Identify the blood parasite species.
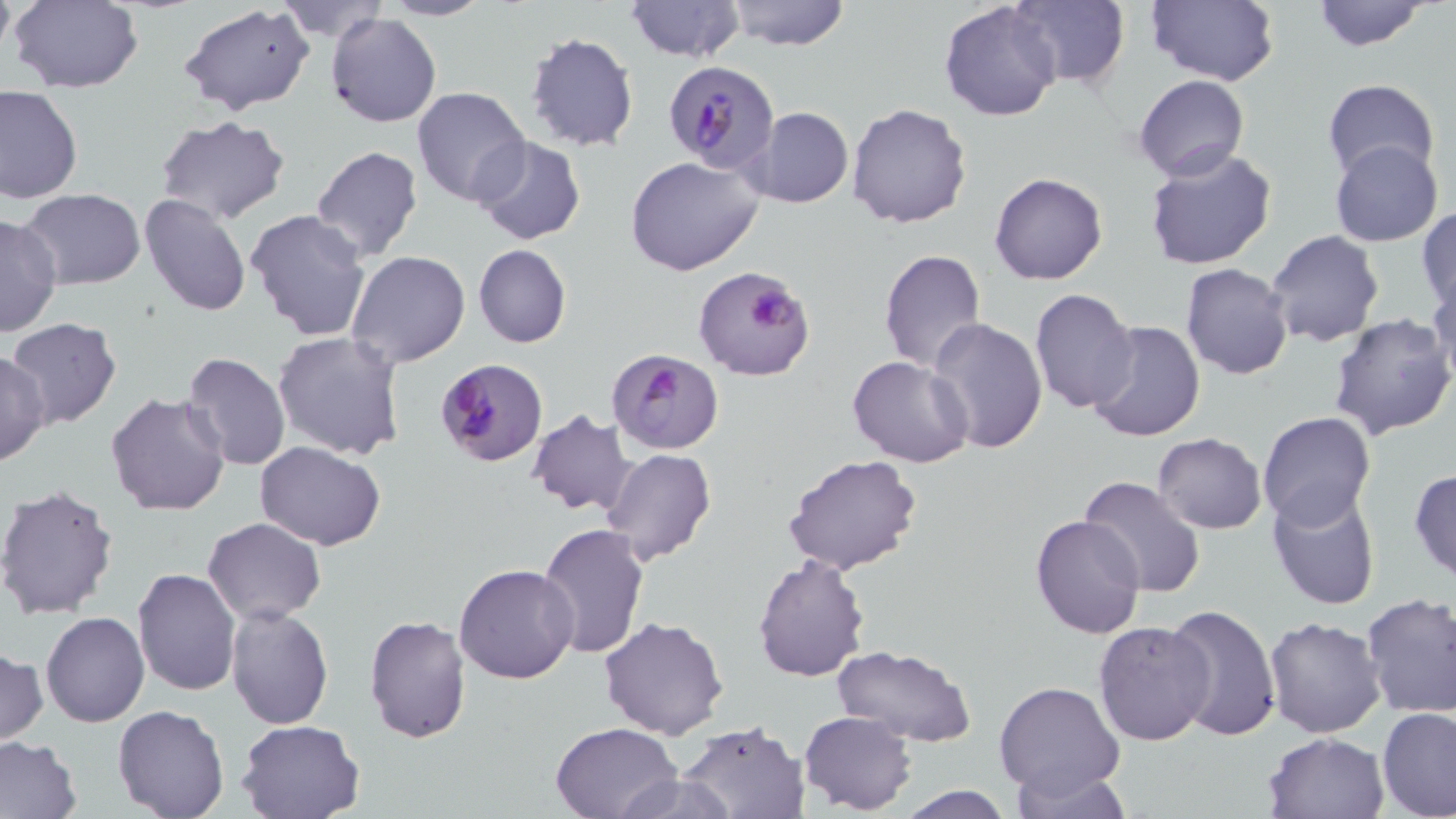

Plasmodium falciparum.

Summary:
  - Coordinate format: approximate bounding boxes as named x1/y1/x2/y2 corners in pixels
  - Uninfected red blood cell locations: (x1=8, y1=0, x2=144, y2=93), (x1=274, y1=0, x2=389, y2=42), (x1=381, y1=0, x2=492, y2=21), (x1=624, y1=0, x2=745, y2=63), (x1=724, y1=0, x2=851, y2=50), (x1=1009, y1=0, x2=1130, y2=88), (x1=1147, y1=0, x2=1279, y2=86), (x1=1310, y1=0, x2=1433, y2=51), (x1=940, y1=1, x2=1063, y2=122), (x1=180, y1=3, x2=316, y2=114), (x1=326, y1=11, x2=442, y2=128), (x1=524, y1=32, x2=638, y2=153), (x1=1135, y1=74, x2=1249, y2=183), (x1=1320, y1=78, x2=1440, y2=183), (x1=0, y1=85, x2=83, y2=204), (x1=412, y1=86, x2=530, y2=208), (x1=846, y1=103, x2=972, y2=229), (x1=741, y1=107, x2=855, y2=208), (x1=155, y1=116, x2=293, y2=224), (x1=470, y1=136, x2=586, y2=245), (x1=1330, y1=139, x2=1443, y2=247), (x1=310, y1=146, x2=424, y2=263), (x1=1144, y1=146, x2=1278, y2=270), (x1=627, y1=157, x2=766, y2=277), (x1=990, y1=172, x2=1108, y2=286), (x1=18, y1=190, x2=148, y2=289), (x1=139, y1=195, x2=252, y2=317), (x1=1417, y1=206, x2=1456, y2=311), (x1=245, y1=208, x2=372, y2=342), (x1=0, y1=213, x2=60, y2=340), (x1=1264, y1=230, x2=1385, y2=348), (x1=473, y1=245, x2=571, y2=348), (x1=878, y1=249, x2=987, y2=372), (x1=346, y1=251, x2=471, y2=369), (x1=1181, y1=262, x2=1294, y2=381), (x1=1431, y1=276, x2=1456, y2=391), (x1=1030, y1=288, x2=1140, y2=412), (x1=1329, y1=313, x2=1456, y2=442), (x1=926, y1=315, x2=1050, y2=454), (x1=7, y1=318, x2=123, y2=429), (x1=1084, y1=318, x2=1207, y2=443), (x1=273, y1=332, x2=407, y2=462), (x1=1, y1=348, x2=50, y2=468), (x1=182, y1=352, x2=291, y2=470), (x1=846, y1=354, x2=973, y2=468), (x1=106, y1=391, x2=232, y2=517), (x1=527, y1=409, x2=637, y2=516), (x1=1258, y1=410, x2=1375, y2=527), (x1=1153, y1=432, x2=1267, y2=534), (x1=255, y1=441, x2=386, y2=549), (x1=602, y1=449, x2=717, y2=566), (x1=782, y1=454, x2=922, y2=575), (x1=1409, y1=468, x2=1456, y2=582), (x1=1079, y1=475, x2=1206, y2=601), (x1=0, y1=484, x2=120, y2=619), (x1=1267, y1=488, x2=1381, y2=612), (x1=1029, y1=515, x2=1147, y2=639), (x1=202, y1=516, x2=326, y2=624), (x1=535, y1=522, x2=650, y2=659), (x1=752, y1=554, x2=871, y2=682), (x1=454, y1=562, x2=581, y2=683), (x1=132, y1=569, x2=242, y2=696), (x1=1359, y1=591, x2=1456, y2=718), (x1=224, y1=603, x2=334, y2=730), (x1=1162, y1=604, x2=1282, y2=742), (x1=41, y1=611, x2=150, y2=729), (x1=363, y1=613, x2=472, y2=744), (x1=599, y1=615, x2=729, y2=739), (x1=1263, y1=616, x2=1386, y2=738), (x1=1092, y1=620, x2=1218, y2=746), (x1=1, y1=645, x2=47, y2=748), (x1=829, y1=645, x2=976, y2=747), (x1=994, y1=679, x2=1127, y2=804), (x1=112, y1=703, x2=232, y2=819), (x1=1376, y1=706, x2=1456, y2=819), (x1=799, y1=711, x2=918, y2=816), (x1=237, y1=718, x2=366, y2=819), (x1=549, y1=721, x2=681, y2=819), (x1=677, y1=721, x2=810, y2=819), (x1=1263, y1=731, x2=1389, y2=818), (x1=0, y1=737, x2=83, y2=818), (x1=1013, y1=771, x2=1140, y2=818), (x1=611, y1=772, x2=738, y2=819), (x1=895, y1=786, x2=1016, y2=818)
  - Plasmodium falciparum-infected red blood cell locations: (x1=664, y1=61, x2=780, y2=174), (x1=691, y1=264, x2=814, y2=382), (x1=607, y1=348, x2=724, y2=456), (x1=435, y1=359, x2=548, y2=467)
  - Stain: May-Grünwald-Giemsa
  - Preparation: thin blood film
  - Modality: light microscopy
  - Magnification: 1000x
  - Image size: 1456×819 pixels
  - Field of view: one of a larger specimen